Evaluate for Plasmodium parasites.
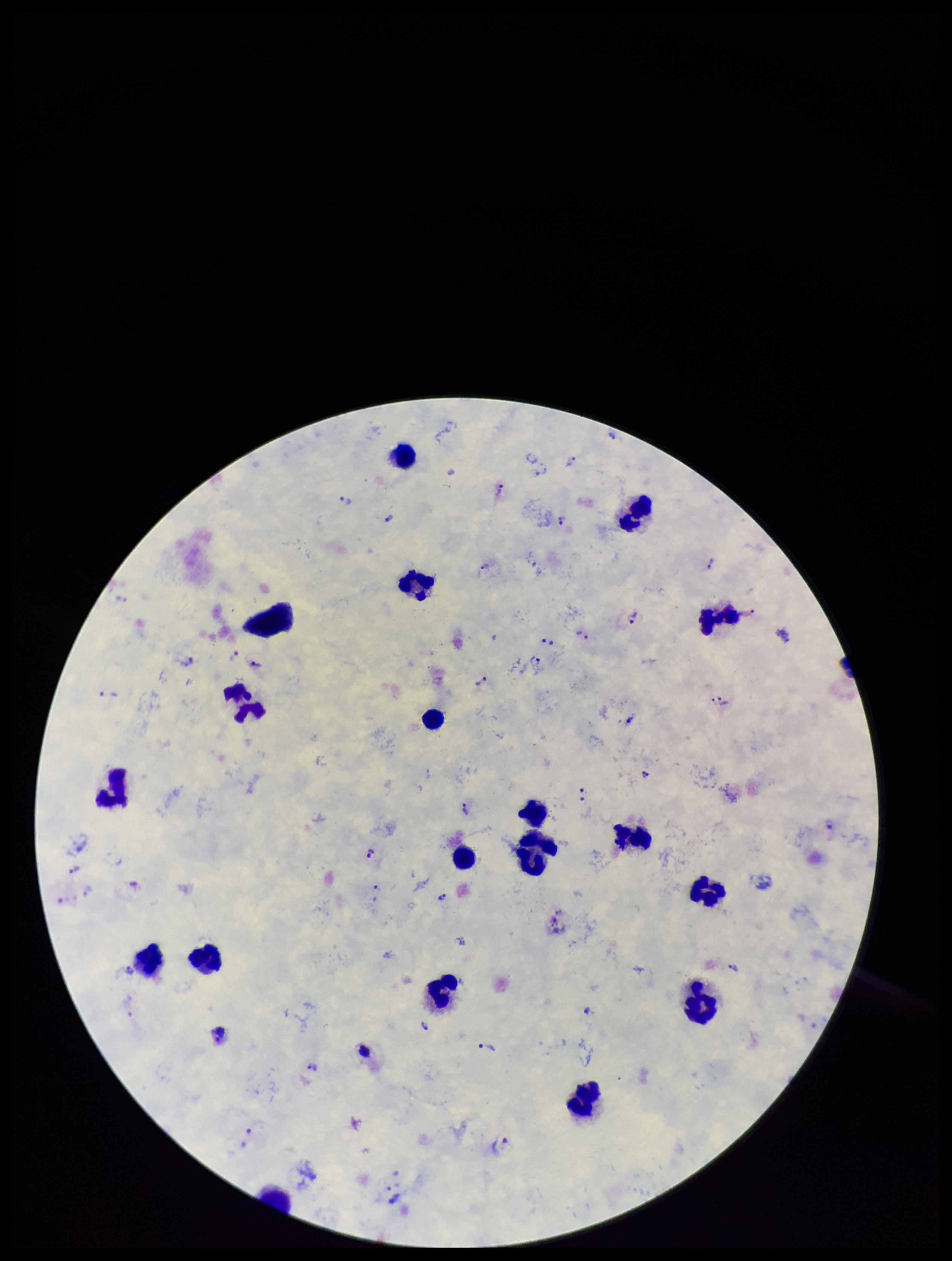

Identified.

Single field of view. Stained with Giemsa. Image is 952×1261 pixels. Smartphone photograph taken through the eyepiece of a microscope. Species reported for this patient: Plasmodium vivax. Leukocyte count: 18. Preparation: thick smear. Parasite count: 41. Patient malaria status: infected.